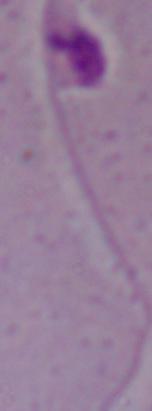 A Leishmania parasite is shown. 1000x magnification. Micrograph.